Give the position of every malaria parasite.
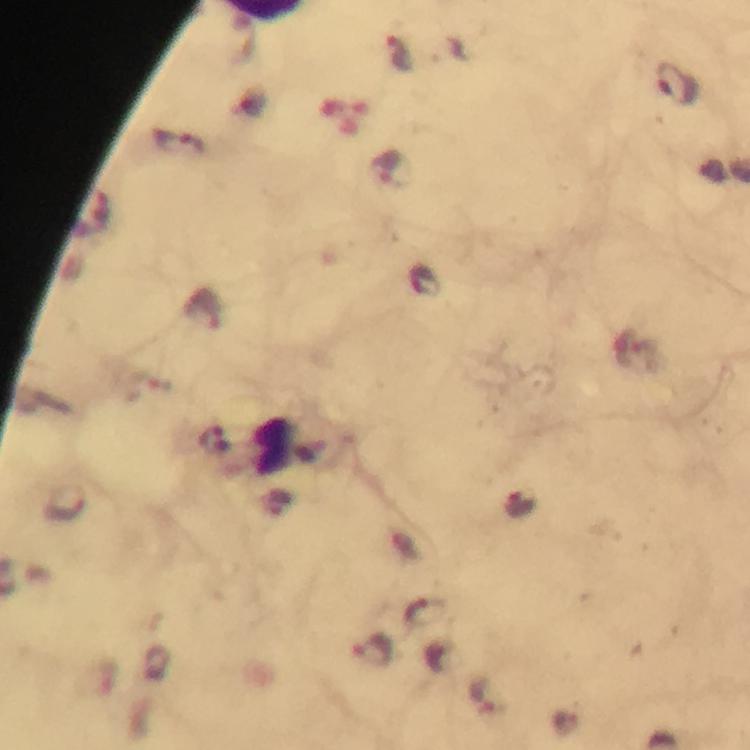

Approximate centers as (x, y) in pixels.
Malaria parasites: (400, 55), (678, 83), (180, 144), (391, 169), (425, 281), (204, 309), (427, 613), (373, 651), (485, 696).

context: from a malaria diagnostic workup
image_size: 750×750 pixels
preparation: thick blood film
stain: Giemsa
magnification: 100x
cropped_from: a single field of view
immersion_oil: used
capture: smartphone photograph through a microscope